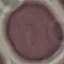
result = no malaria parasites seen
image type = cell patch, automatically extracted from a larger field of view and resized to 64 × 64 pixels
capture = smartphone through the microscope eyepiece
stain = Giemsa
preparation = thin blood film